Give the extent of all Plasmodium ovale-infected red blood cells.
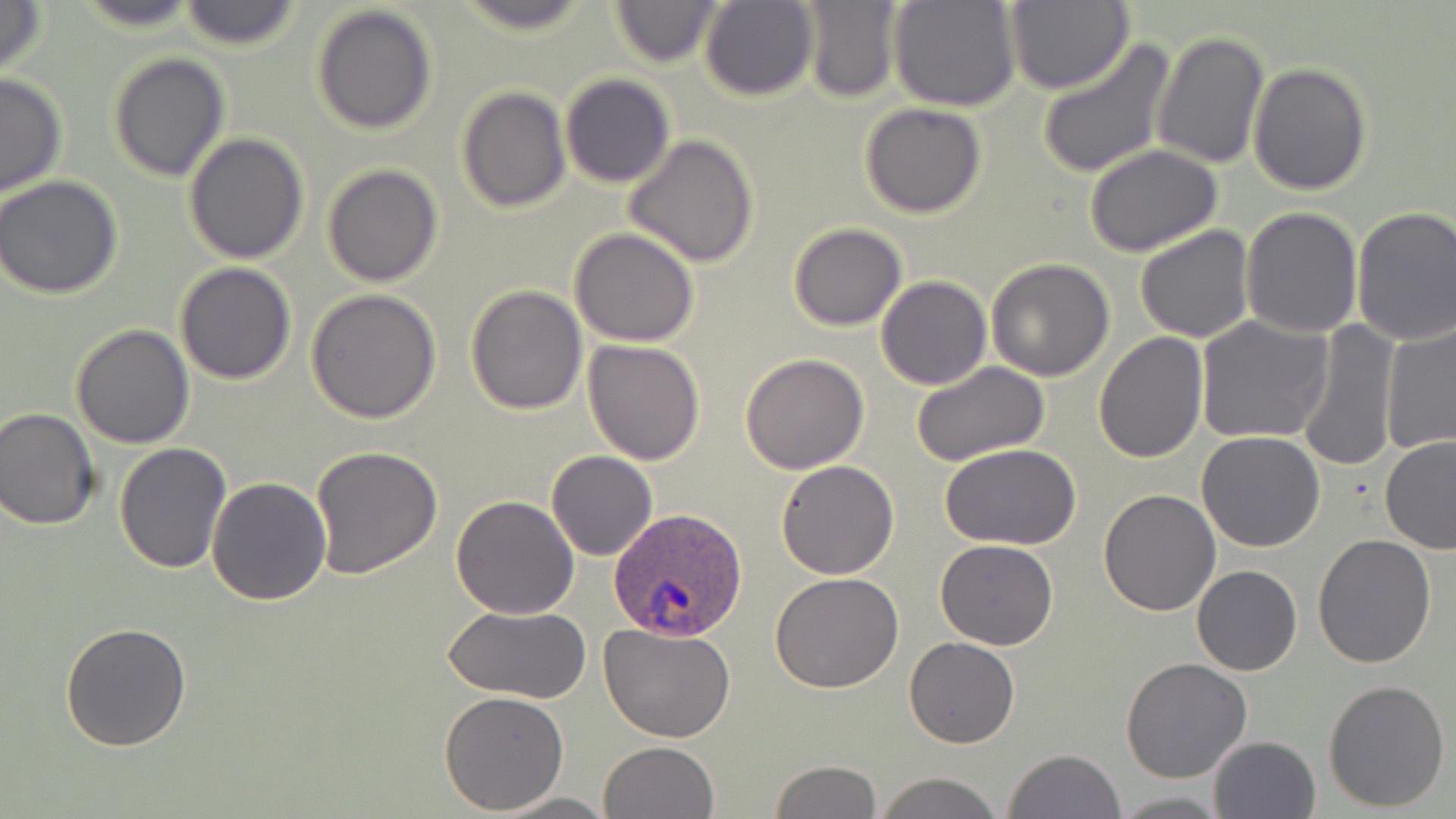
Approximate bounding boxes as (x1,y1)-(x2,y2) corner pairs in pixels.
Plasmodium ovale-infected red blood cells: (609,507)-(746,644).

Summary:
  - Uninfected red blood cell locations: (72,0)-(205,29), (607,0)-(727,68), (698,0)-(818,102), (889,0)-(1020,112), (0,1)-(48,80), (177,1)-(304,52), (799,1)-(903,102), (1006,1)-(1133,96), (449,2)-(597,35), (310,4)-(439,136), (1151,29)-(1269,169), (1036,39)-(1175,178), (107,52)-(230,182), (1248,62)-(1371,195), (0,72)-(68,198), (560,74)-(674,189), (457,86)-(571,213), (859,102)-(985,218), (184,133)-(311,265), (623,133)-(760,268), (1084,146)-(1223,256), (321,165)-(443,287), (1,175)-(124,299), (1351,205)-(1456,346), (1241,207)-(1363,339), (786,222)-(908,331), (1134,225)-(1255,344), (570,228)-(699,348), (985,259)-(1115,382), (174,262)-(298,385), (876,275)-(991,390), (465,284)-(588,414), (306,290)-(442,426), (1195,315)-(1331,445), (1293,320)-(1403,472), (1379,322)-(1456,455), (70,323)-(196,448), (1094,331)-(1209,464), (583,340)-(706,465), (740,353)-(870,474), (910,360)-(1051,466), (0,407)-(101,530), (1197,431)-(1326,552), (1379,436)-(1456,556), (114,441)-(232,574), (940,443)-(1084,548), (309,445)-(442,579), (546,450)-(657,561), (775,459)-(900,579), (206,478)-(332,605), (1098,487)-(1221,615), (450,495)-(579,619), (1311,536)-(1436,668), (934,538)-(1059,651), (1192,565)-(1302,676), (770,571)-(904,694), (442,605)-(590,702), (61,621)-(193,753), (599,621)-(736,742), (905,637)-(1019,749), (1119,657)-(1252,784), (1323,678)-(1451,813), (438,690)-(569,813), (1208,735)-(1321,819), (598,741)-(721,819), (1003,748)-(1127,819), (769,760)-(882,818), (873,773)-(1005,819), (494,792)-(615,818), (1111,792)-(1226,817)
  - Slide-level diagnosis: Plasmodium ovale
  - Modality: light microscopy
  - Stain: May-Grünwald-Giemsa
  - Image size: 1456×819 pixels
  - Field of view: single
  - Magnification: 1000x
  - Preparation: thin blood smear